Point out each Plasmodium parasite.
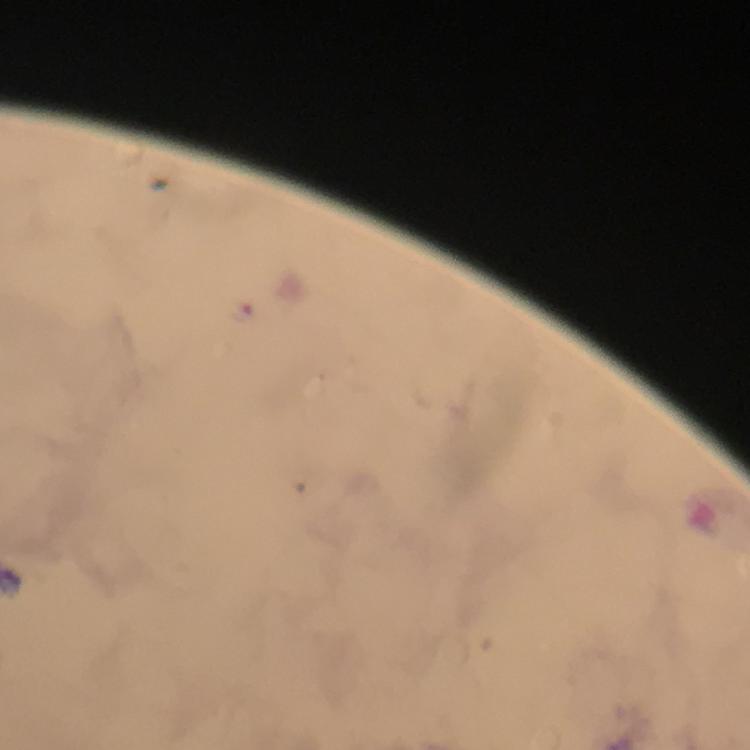

Approximate centers as (x, y) in pixels.
Plasmodium parasites: (243, 312).

100x magnification. Image is 750×750 pixels. Smartphone photograph taken through a microscope. Giemsa-stained preparation. Immersion oil applied. Cropped region of a single field of view. From a diagnostic examination for malaria. Thick blood film.